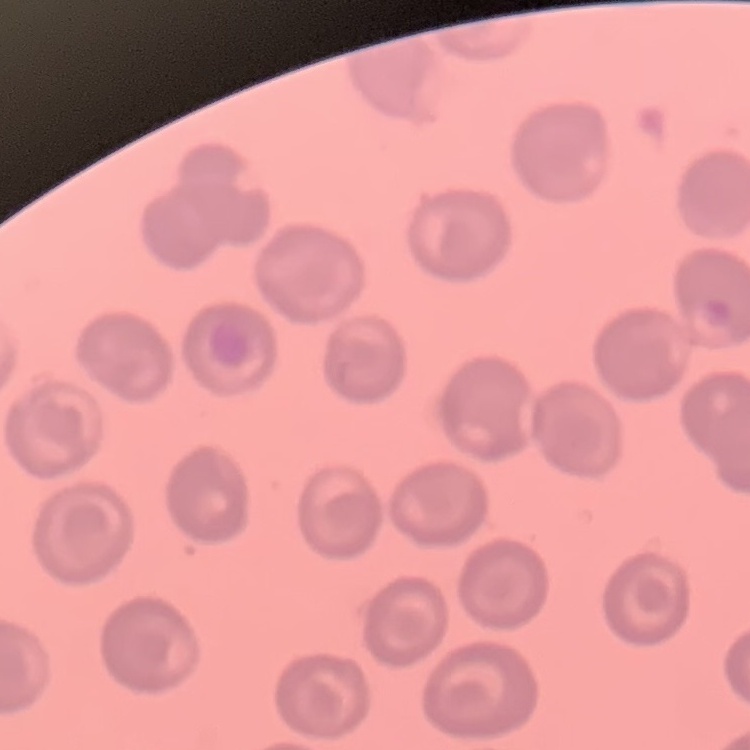
The erythrocytes exhibit no rouleaux formation. Thin blood smear. Square crop of a larger photomicrograph. Stained with either Field's or Giemsa.